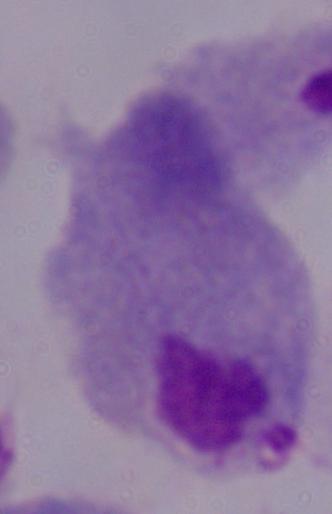

Summary:
  - Magnification: 1000x
  - Identification: trichomonad
  - Modality: photomicrograph